Name the parasite shown.
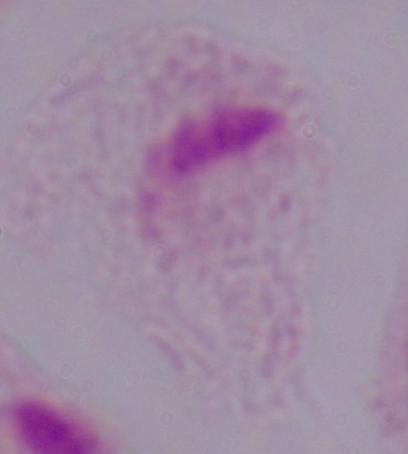
A trichomonad.

magnification = 1000x
modality = photomicrograph